Give the extent of all uninfected red blood cells.
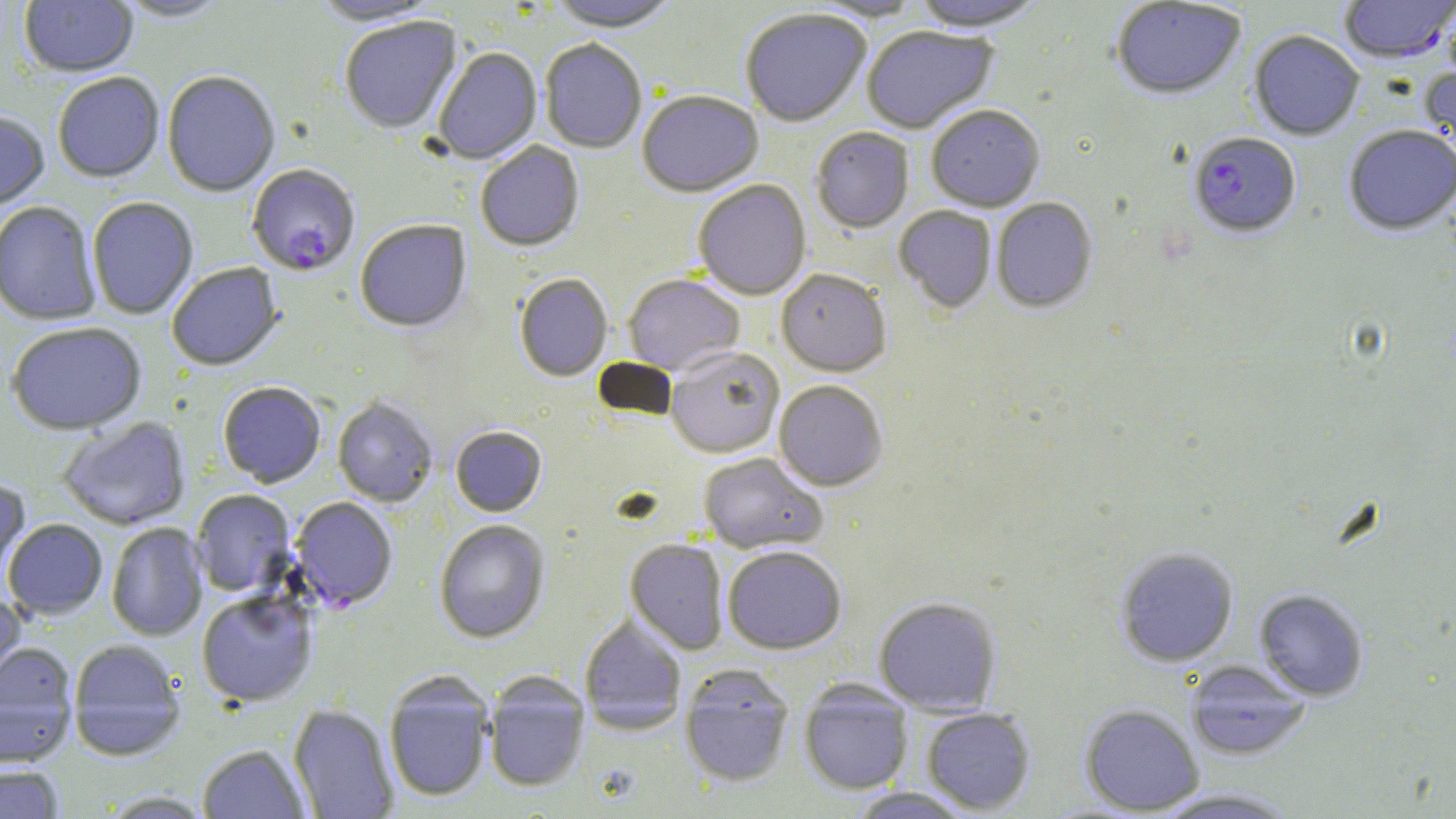
Approximate bounding boxes as [x1, y1, x2, y2] in pixels.
Uninfected red blood cells: [19, 0, 139, 79], [112, 0, 232, 23], [309, 0, 445, 26], [545, 0, 682, 33], [805, 0, 927, 22], [910, 0, 1049, 34], [1111, 1, 1247, 101], [740, 9, 872, 127], [339, 17, 461, 134], [862, 27, 998, 135], [1249, 31, 1364, 141], [540, 40, 647, 154], [432, 48, 542, 164], [1419, 53, 1456, 174], [162, 71, 280, 197], [52, 73, 165, 184], [637, 91, 763, 198], [926, 106, 1045, 213], [0, 111, 49, 211], [1343, 126, 1456, 237], [811, 128, 914, 234], [475, 141, 585, 251], [693, 180, 812, 300], [87, 197, 198, 319], [991, 198, 1098, 313], [0, 202, 102, 326], [894, 206, 997, 313], [355, 220, 471, 333], [167, 263, 283, 371], [776, 268, 891, 377], [514, 273, 613, 381], [623, 274, 745, 376], [7, 322, 147, 434], [665, 346, 785, 458], [774, 379, 888, 491], [217, 381, 326, 488], [332, 397, 438, 507], [56, 416, 192, 530], [450, 426, 547, 516], [697, 451, 828, 553], [0, 481, 31, 589], [191, 489, 295, 597], [2, 519, 108, 619], [434, 519, 550, 643], [106, 522, 208, 641], [625, 539, 729, 654], [722, 544, 847, 654], [1115, 546, 1239, 667], [0, 589, 27, 698], [1254, 589, 1368, 701], [196, 591, 318, 707], [873, 595, 1002, 715], [579, 614, 688, 733], [68, 640, 186, 759], [0, 642, 79, 766], [1185, 662, 1312, 760], [679, 667, 796, 788], [383, 673, 495, 802], [483, 674, 589, 792], [798, 683, 915, 795], [289, 703, 399, 818], [1079, 704, 1205, 816], [922, 707, 1035, 814], [198, 744, 310, 818], [0, 764, 65, 819], [844, 787, 979, 818], [1147, 787, 1303, 818], [97, 790, 217, 818].

Summary:
  - Plasmodium falciparum-infected red blood cell locations: [1339, 0, 1455, 65], [1188, 132, 1301, 238], [247, 165, 360, 277], [290, 497, 398, 611]
  - Slide-level diagnosis: Plasmodium falciparum
  - Image size: 1456×819 pixels
  - Field of view: one of a larger specimen
  - Preparation: thin blood film
  - Stain: May-Grünwald-Giemsa
  - Modality: optical microscopy
  - Magnification: 1000x